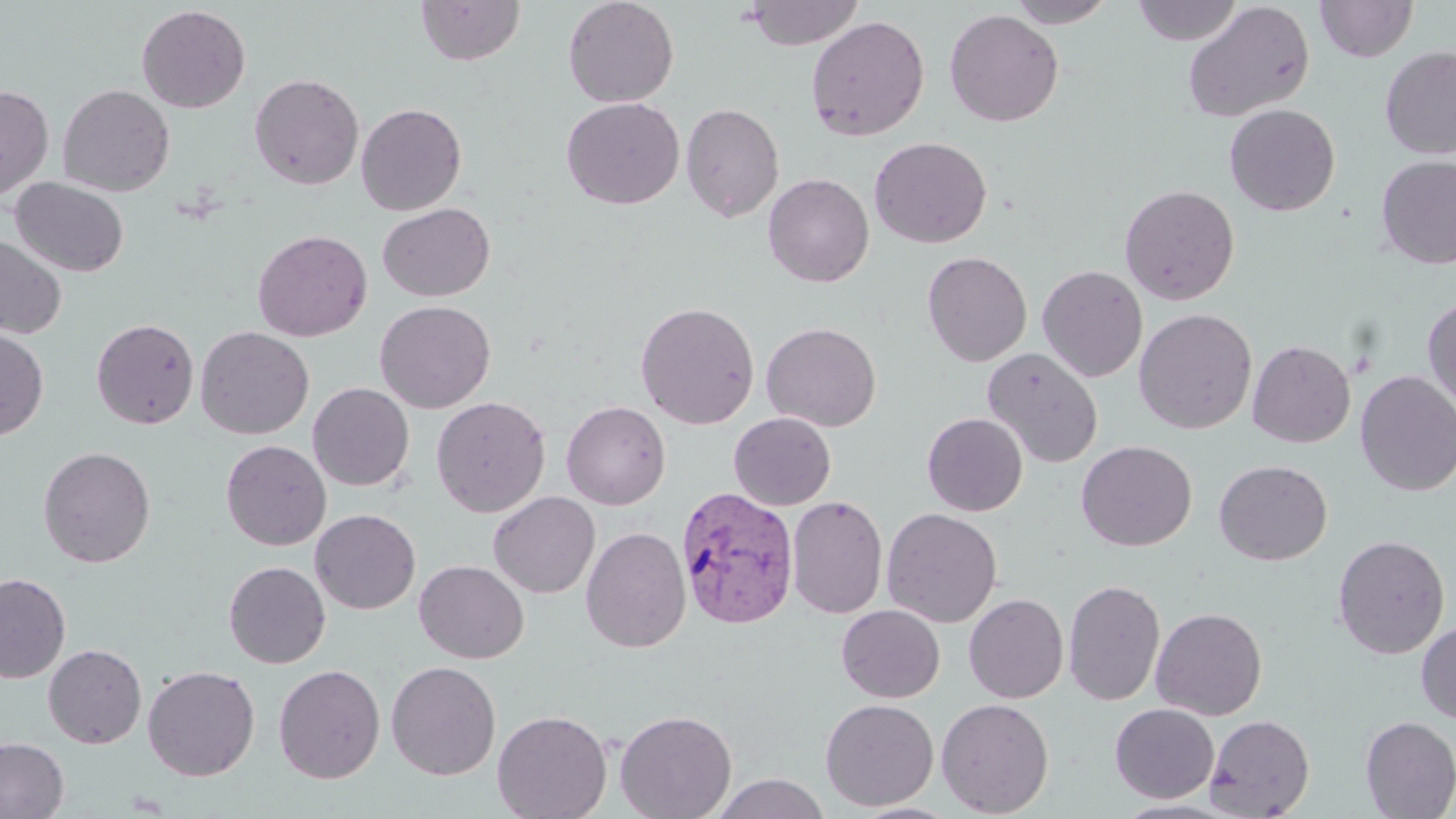

{
  "slide_level_diagnosis": "Plasmodium vivax",
  "magnification": "1000x",
  "plasmodium_vivax_infected_red_blood_cell_locations": "approximate bounding boxes as [x1, y1, x2, y2] in pixels: [676, 486, 800, 631]",
  "modality": "optical microscopy",
  "image_size": "1456×819 pixels",
  "uninfected_red_blood_cell_locations": "approximate bounding boxes as [x1, y1, x2, y2] in pixels: [415, 0, 525, 66], [563, 0, 680, 108], [744, 0, 865, 50], [1006, 0, 1116, 27], [1132, 0, 1243, 45], [1182, 1, 1315, 122], [1315, 1, 1419, 62], [136, 5, 251, 113], [944, 8, 1064, 127], [805, 15, 930, 142], [1380, 45, 1456, 159], [249, 73, 364, 190], [0, 83, 54, 203], [57, 84, 175, 197], [561, 97, 684, 209], [681, 102, 785, 222], [356, 103, 467, 215], [1224, 104, 1340, 216], [869, 136, 992, 248], [1375, 155, 1456, 269], [762, 173, 874, 287], [10, 177, 129, 277], [1120, 184, 1240, 305], [1128, 185, 1245, 438], [377, 202, 495, 302], [252, 229, 372, 342], [0, 234, 68, 339], [922, 251, 1032, 366], [1037, 265, 1148, 382], [1422, 294, 1456, 417], [374, 300, 497, 412], [635, 301, 760, 429], [1134, 308, 1257, 434], [91, 318, 199, 430], [761, 321, 882, 432], [195, 326, 314, 440], [0, 327, 49, 440], [1247, 340, 1356, 448], [982, 347, 1104, 468], [1355, 370, 1456, 496], [307, 383, 414, 491], [431, 396, 551, 517], [561, 401, 670, 510], [729, 412, 836, 510], [922, 413, 1028, 516], [221, 440, 331, 550], [1076, 440, 1197, 551], [38, 446, 156, 568], [1214, 460, 1332, 565], [488, 491, 600, 598], [786, 495, 888, 619], [310, 508, 421, 614], [881, 508, 1002, 627], [580, 526, 691, 653], [1332, 534, 1450, 659], [223, 560, 331, 668], [414, 560, 529, 664], [0, 571, 71, 683], [1063, 578, 1166, 707], [963, 594, 1069, 703], [836, 604, 945, 703], [1151, 607, 1267, 720], [1416, 620, 1456, 724], [43, 644, 147, 748], [386, 660, 501, 780], [273, 663, 385, 783], [142, 665, 260, 781], [820, 698, 939, 811], [936, 698, 1054, 817], [1109, 703, 1219, 803], [492, 709, 612, 819], [614, 709, 737, 819], [1204, 714, 1315, 818], [1359, 716, 1456, 818], [0, 736, 69, 819], [710, 773, 830, 818]",
  "stain": "May-Grünwald-Giemsa",
  "preparation": "thin blood film",
  "field_of_view": "single"
}